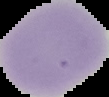
result = negative for Plasmodium parasites
image type = cell region segmented out of the field of view; surrounding area masked to black
image size = 109×97 pixels
preparation = thin blood smear